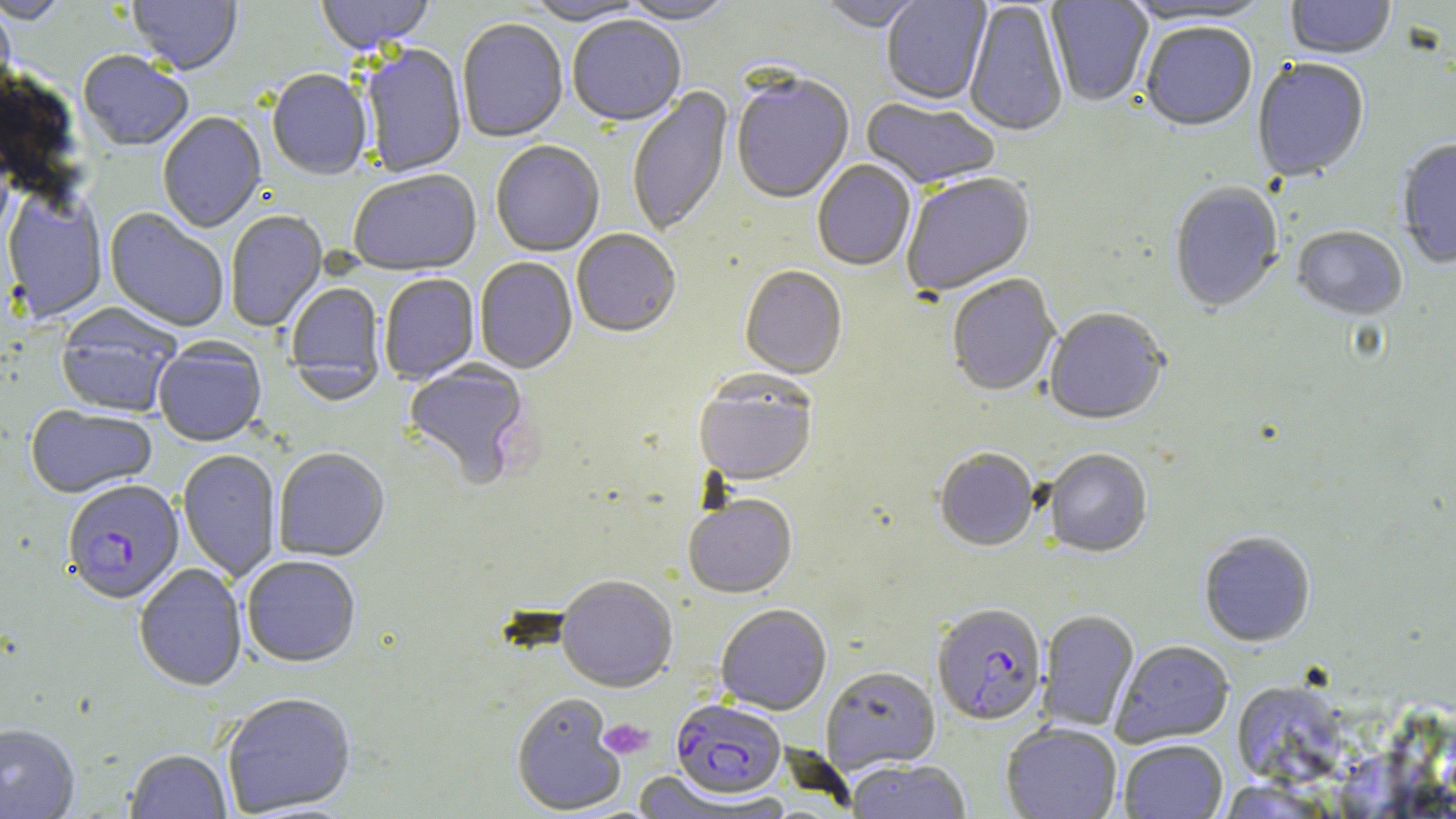

Summary:
  - Coordinate format: approximate bounding boxes as [x1, y1, x2, y2] in pixels
  - Plasmodium falciparum-infected red blood cell locations: [62, 481, 184, 607], [932, 603, 1046, 726], [671, 700, 786, 800]
  - Platelet locations: [599, 718, 654, 760]
  - Uninfected red blood cell locations: [1, 0, 71, 26], [127, 0, 243, 77], [316, 0, 435, 57], [519, 0, 648, 27], [618, 0, 736, 27], [881, 0, 992, 107], [1046, 0, 1154, 108], [1285, 0, 1396, 62], [819, 1, 927, 33], [1119, 1, 1276, 27], [964, 2, 1068, 138], [0, 4, 16, 98], [568, 18, 686, 130], [457, 20, 568, 144], [1140, 24, 1257, 134], [359, 45, 467, 178], [77, 53, 193, 153], [1252, 60, 1369, 184], [267, 71, 373, 182], [731, 75, 854, 206], [627, 86, 733, 238], [860, 99, 999, 191], [157, 113, 267, 234], [1397, 140, 1456, 270], [490, 142, 605, 258], [812, 161, 916, 272], [348, 171, 482, 278], [901, 173, 1037, 298], [1169, 183, 1285, 315], [2, 190, 108, 325], [104, 208, 229, 332], [225, 210, 328, 332], [1292, 228, 1407, 322], [572, 231, 681, 339], [475, 258, 577, 374], [739, 267, 847, 380], [379, 274, 479, 385], [947, 276, 1060, 398], [285, 284, 386, 403], [55, 307, 181, 419], [1045, 309, 1168, 426], [153, 341, 266, 448], [403, 361, 531, 488], [694, 375, 817, 487], [25, 406, 157, 500], [177, 449, 281, 583], [274, 449, 389, 562], [934, 449, 1038, 552], [1044, 450, 1152, 558], [684, 496, 797, 599], [1199, 532, 1315, 648], [242, 556, 361, 668], [134, 563, 247, 693], [556, 577, 678, 693], [716, 605, 832, 715], [1037, 609, 1139, 733], [1112, 640, 1234, 747], [821, 666, 940, 773], [1231, 681, 1350, 789], [511, 693, 626, 816], [222, 694, 357, 817], [1001, 723, 1121, 819], [0, 724, 80, 818], [1119, 739, 1228, 819], [125, 750, 232, 819], [847, 760, 971, 818], [628, 771, 759, 817]
  - Slide-level diagnosis: Plasmodium falciparum
  - Image size: 1456×819 pixels
  - Preparation: thin blood smear
  - Modality: optical microscopy
  - Field of view: one of a larger specimen
  - Magnification: 1000x
  - Stain: May-Grünwald-Giemsa